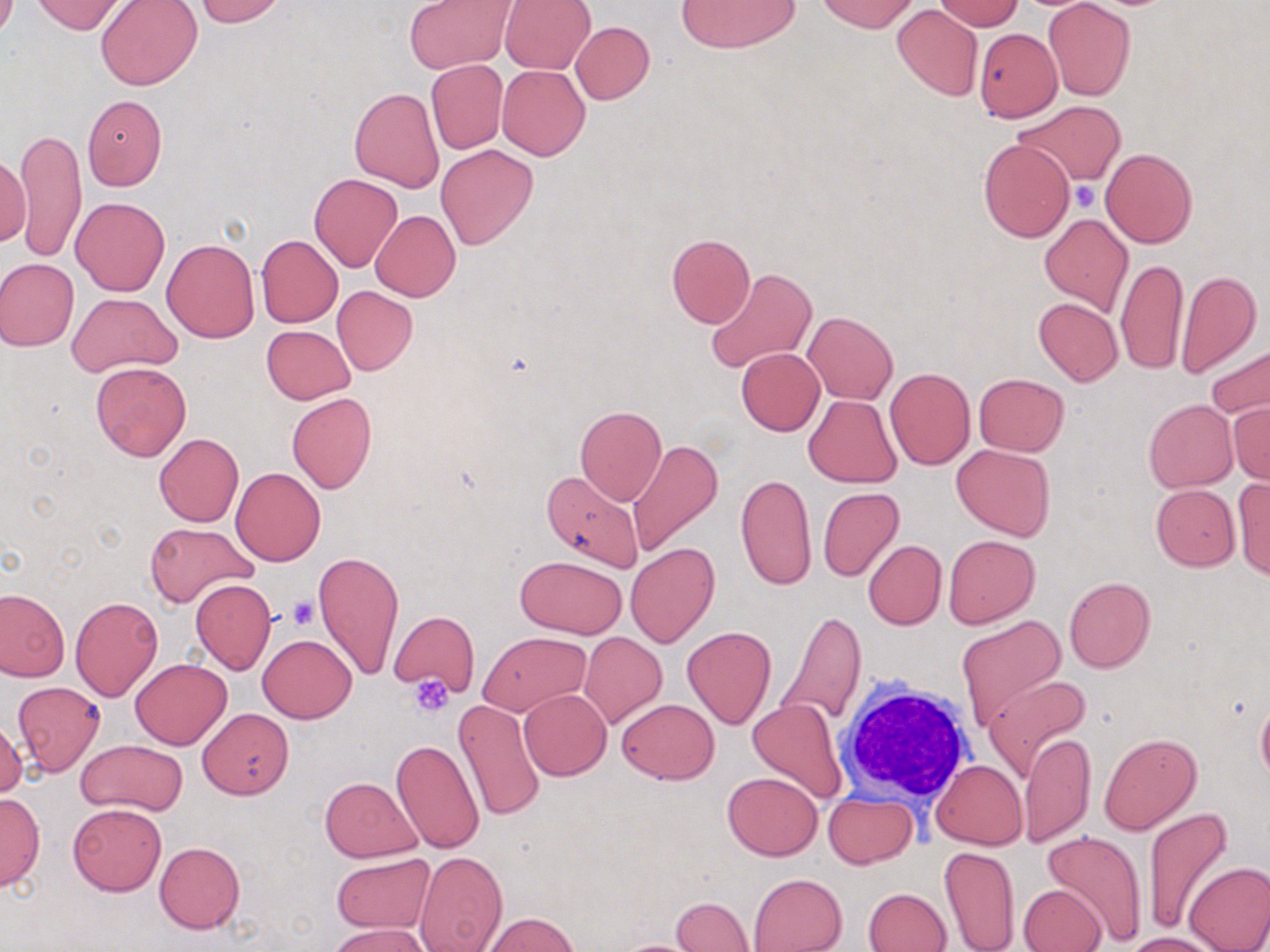
slide-level diagnosis = no evidence of blood parasites
platelet locations = approximate bounding boxes as [x1, y1, x2, y2] in pixels: [1071, 183, 1099, 212], [288, 596, 319, 630], [409, 675, 456, 719]
preparation = thin blood smear
white blood cell locations = approximate bounding boxes as [x1, y1, x2, y2] in pixels: [836, 676, 978, 809]
modality = light microscopy
magnification = 1000x
stain = May-Grünwald-Giemsa
field of view = one of a larger specimen
uninfected red blood cell locations = approximate bounding boxes as [x1, y1, x2, y2] in pixels: [31, 0, 128, 34], [196, 0, 285, 26], [500, 0, 595, 74], [817, 0, 918, 33], [96, 1, 203, 90], [406, 1, 513, 73], [676, 1, 800, 52], [933, 1, 1025, 31], [1042, 1, 1136, 101], [893, 4, 983, 100], [570, 22, 654, 104], [973, 26, 1063, 123], [425, 59, 508, 154], [497, 66, 590, 160], [349, 87, 445, 192], [81, 94, 165, 190], [1015, 101, 1126, 185], [13, 127, 86, 263], [979, 138, 1074, 241], [436, 144, 537, 249], [1101, 147, 1197, 248], [0, 153, 32, 247], [309, 174, 402, 272], [71, 197, 171, 296], [370, 211, 460, 303], [1039, 213, 1133, 316], [256, 235, 342, 327], [665, 235, 755, 328], [163, 239, 259, 342], [1115, 257, 1187, 374], [0, 258, 79, 351], [704, 266, 817, 375], [1175, 270, 1262, 377], [332, 286, 417, 374], [66, 293, 181, 376], [1033, 299, 1122, 386], [803, 311, 898, 404], [261, 325, 355, 404], [1205, 342, 1270, 421], [736, 348, 825, 436], [91, 362, 191, 460], [885, 367, 975, 469], [973, 373, 1068, 456], [286, 393, 377, 493], [804, 395, 901, 486], [1144, 399, 1237, 491], [1226, 401, 1270, 484], [575, 405, 667, 507], [153, 433, 243, 527], [627, 439, 724, 557], [952, 443, 1055, 541], [231, 467, 326, 566], [542, 469, 645, 573], [736, 472, 816, 591], [1231, 477, 1270, 579], [1150, 484, 1239, 571], [817, 487, 904, 582], [145, 521, 256, 607], [943, 534, 1039, 629], [863, 539, 947, 630], [625, 543, 718, 648], [313, 550, 405, 680], [514, 555, 628, 638], [1064, 576, 1155, 672], [191, 578, 276, 673], [0, 589, 69, 681], [70, 596, 162, 701], [389, 610, 478, 697], [777, 610, 866, 732], [955, 616, 1067, 730], [681, 626, 777, 728], [478, 631, 590, 716], [579, 632, 667, 728], [257, 633, 356, 722], [130, 658, 233, 749], [985, 674, 1091, 780], [12, 681, 104, 775], [519, 689, 612, 779], [615, 697, 719, 785], [454, 699, 545, 822], [749, 699, 848, 802], [197, 707, 294, 799], [0, 714, 27, 801], [1020, 730, 1095, 849], [1098, 733, 1201, 835], [76, 739, 187, 816], [391, 739, 485, 856], [931, 759, 1027, 850], [722, 771, 822, 860], [320, 776, 422, 862], [0, 791, 44, 890], [824, 791, 917, 867], [67, 803, 166, 895], [1144, 805, 1234, 937], [1042, 830, 1148, 945], [155, 842, 245, 933], [938, 845, 1021, 952], [414, 849, 508, 952], [330, 852, 436, 935], [1183, 861, 1270, 952], [748, 873, 848, 952], [1018, 883, 1107, 952], [864, 887, 951, 952], [672, 895, 754, 951], [481, 913, 579, 951], [328, 923, 433, 952], [1122, 932, 1222, 951]
image size = 1270×952 pixels